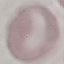
Malaria status: uninfected. Photographed with a smartphone camera at the microscope eyepiece. Giemsa-stained preparation. Automatically extracted cell patch, resized to 64 × 64 pixels. Thin blood film.